Assess this cell for malaria.
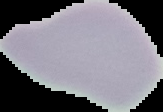

Uninfected.

Summary:
  - Image type: cell region segmented out of the field of view; surrounding area masked to black
  - Preparation: thin blood smear
  - Image size: 163×112 pixels